State the blood parasite species.
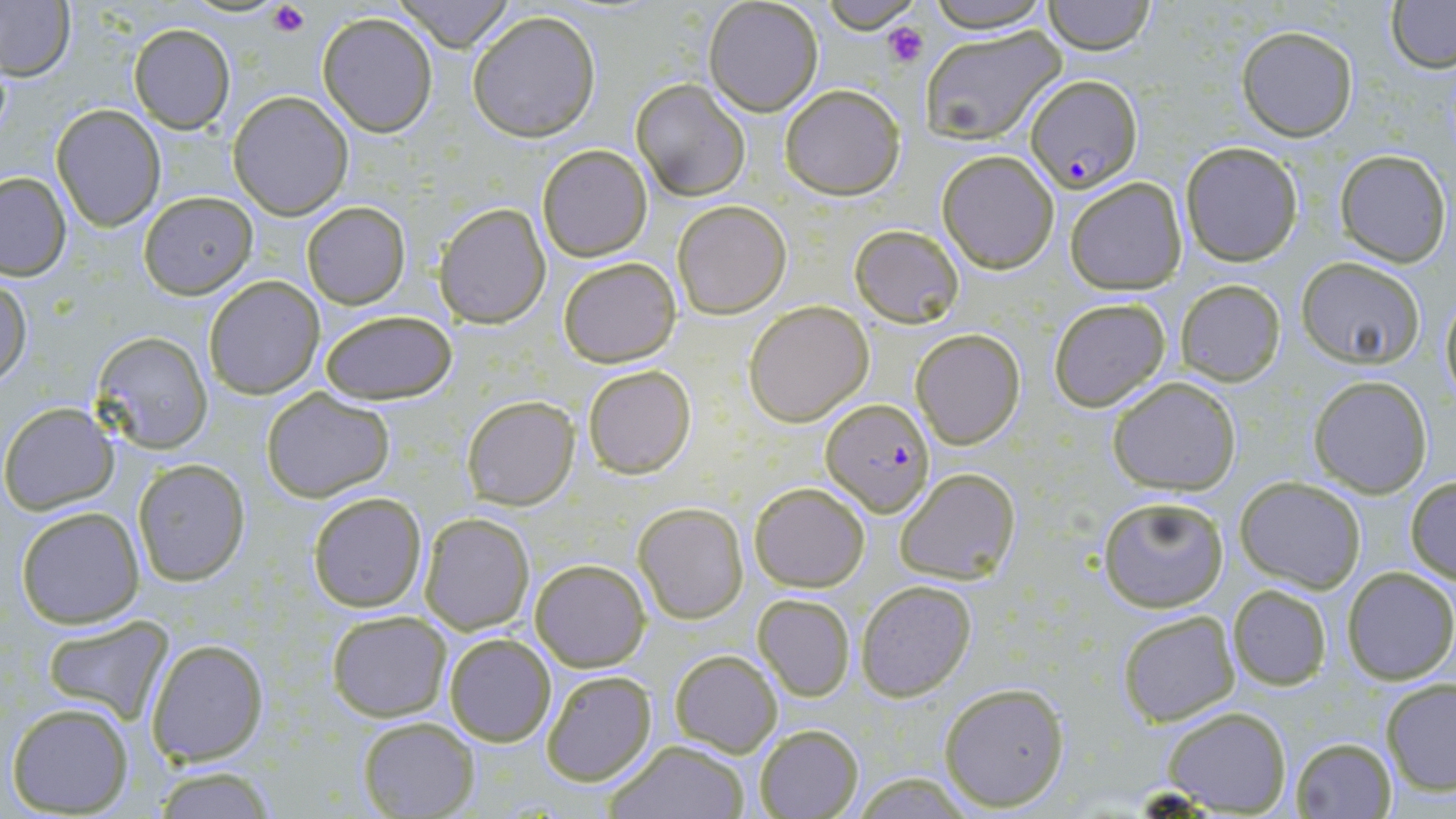

Plasmodium falciparum.

Approximate bounding boxes as named x1/y1/x2/y2 corners in pixels. Plasmodium falciparum-infected red blood cell locations: (x1=1025, y1=74, x2=1143, y2=192), (x1=823, y1=399, x2=936, y2=518). Uninfected red blood cell locations: (x1=391, y1=0, x2=514, y2=50), (x1=702, y1=0, x2=823, y2=117), (x1=820, y1=0, x2=920, y2=33), (x1=924, y1=0, x2=1054, y2=34), (x1=1386, y1=0, x2=1456, y2=71), (x1=0, y1=1, x2=76, y2=82), (x1=1042, y1=1, x2=1157, y2=54), (x1=467, y1=9, x2=602, y2=142), (x1=317, y1=12, x2=438, y2=136), (x1=129, y1=24, x2=236, y2=133), (x1=919, y1=24, x2=1067, y2=145), (x1=1237, y1=26, x2=1358, y2=140), (x1=629, y1=79, x2=752, y2=202), (x1=780, y1=83, x2=904, y2=199), (x1=229, y1=92, x2=353, y2=218), (x1=52, y1=104, x2=166, y2=231), (x1=1180, y1=142, x2=1303, y2=265), (x1=535, y1=144, x2=652, y2=261), (x1=1334, y1=148, x2=1451, y2=265), (x1=937, y1=151, x2=1059, y2=273), (x1=0, y1=172, x2=71, y2=280), (x1=1064, y1=176, x2=1188, y2=295), (x1=139, y1=191, x2=257, y2=298), (x1=673, y1=200, x2=791, y2=318), (x1=302, y1=202, x2=409, y2=309), (x1=435, y1=203, x2=551, y2=328), (x1=849, y1=223, x2=965, y2=329), (x1=558, y1=256, x2=680, y2=368), (x1=1296, y1=257, x2=1427, y2=367), (x1=203, y1=275, x2=324, y2=399), (x1=0, y1=276, x2=32, y2=387), (x1=1174, y1=281, x2=1286, y2=385), (x1=1438, y1=289, x2=1456, y2=411), (x1=1049, y1=297, x2=1172, y2=411), (x1=744, y1=300, x2=873, y2=426), (x1=317, y1=309, x2=458, y2=405), (x1=911, y1=329, x2=1025, y2=449), (x1=92, y1=332, x2=214, y2=453), (x1=583, y1=364, x2=697, y2=480), (x1=1108, y1=376, x2=1241, y2=495), (x1=1309, y1=376, x2=1431, y2=497), (x1=261, y1=386, x2=394, y2=502), (x1=462, y1=395, x2=579, y2=509), (x1=2, y1=403, x2=116, y2=513), (x1=132, y1=458, x2=249, y2=585), (x1=894, y1=466, x2=1022, y2=584), (x1=1405, y1=475, x2=1456, y2=583), (x1=1235, y1=476, x2=1367, y2=590), (x1=748, y1=481, x2=870, y2=590), (x1=307, y1=491, x2=427, y2=612), (x1=1097, y1=495, x2=1230, y2=612), (x1=633, y1=501, x2=748, y2=623), (x1=14, y1=505, x2=145, y2=628), (x1=419, y1=511, x2=535, y2=635), (x1=531, y1=559, x2=649, y2=671), (x1=1342, y1=567, x2=1456, y2=683), (x1=856, y1=578, x2=978, y2=701), (x1=1226, y1=584, x2=1333, y2=691), (x1=754, y1=594, x2=855, y2=702), (x1=1116, y1=609, x2=1241, y2=726), (x1=325, y1=610, x2=452, y2=721), (x1=39, y1=616, x2=174, y2=724), (x1=444, y1=632, x2=557, y2=747), (x1=147, y1=638, x2=270, y2=766), (x1=668, y1=650, x2=783, y2=757), (x1=541, y1=671, x2=656, y2=786), (x1=1380, y1=679, x2=1456, y2=798), (x1=938, y1=681, x2=1070, y2=812), (x1=7, y1=703, x2=134, y2=816), (x1=1162, y1=706, x2=1291, y2=814), (x1=358, y1=717, x2=479, y2=818), (x1=752, y1=723, x2=865, y2=818), (x1=1290, y1=737, x2=1397, y2=818), (x1=605, y1=739, x2=753, y2=818), (x1=150, y1=766, x2=281, y2=818). Platelet locations: (x1=267, y1=3, x2=309, y2=36), (x1=884, y1=21, x2=927, y2=67). Image is 1456×819 pixels. May-Grünwald-Giemsa-stained preparation. Thin blood film. 1000x magnification. One field of a larger specimen. Light microscopy.